Classify this cell by malaria status.
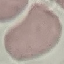
It is uninfected.

{
  "capture": "smartphone camera at the microscope eyepiece",
  "stain": "Giemsa",
  "image_type": "cell patch, automatically extracted from a larger field of view and resized to 64 × 64 pixels",
  "preparation": "thin blood smear"
}